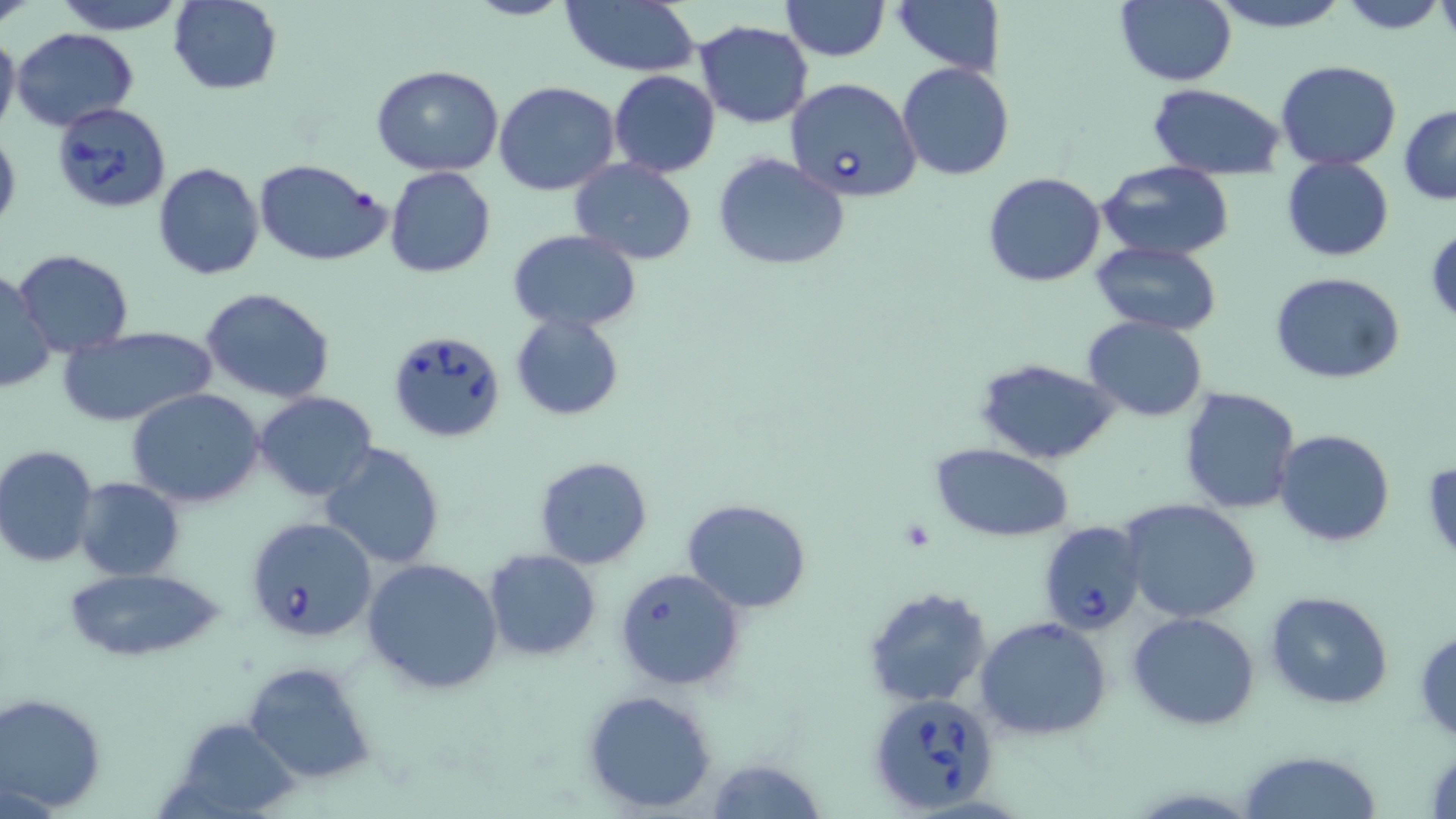
Approximate bounding boxes as (x1,y1)-(x2,y2) corner pairs in pixels. Uninfected red blood cell locations: (0,0)-(36,27), (50,0)-(191,35), (168,0)-(283,94), (465,0)-(571,22), (780,0)-(888,61), (893,0)-(1005,75), (1115,0)-(1237,86), (1204,0)-(1352,33), (1338,0)-(1449,34), (559,2)-(702,77), (693,20)-(814,128), (0,27)-(21,141), (10,27)-(140,132), (1276,59)-(1402,169), (897,62)-(1015,182), (371,65)-(505,177), (609,70)-(720,178), (494,81)-(621,196), (1148,84)-(1285,180), (1398,105)-(1456,204), (714,153)-(849,271), (1282,157)-(1393,262), (254,159)-(392,267), (153,160)-(264,281), (571,160)-(698,264), (1096,160)-(1235,262), (385,167)-(496,279), (984,173)-(1106,288), (1425,225)-(1456,330), (507,229)-(642,334), (1091,240)-(1223,337), (12,249)-(135,356), (0,268)-(56,397), (1270,270)-(1406,385), (200,288)-(335,404), (510,311)-(626,421), (1083,315)-(1207,420), (58,325)-(217,429), (974,358)-(1118,464), (125,387)-(265,509), (1177,387)-(1301,515), (256,391)-(378,502), (1272,429)-(1397,547), (319,441)-(445,570), (932,443)-(1074,542), (1,444)-(100,567), (534,456)-(653,569), (73,477)-(186,581), (681,498)-(811,612), (1118,498)-(1261,622), (483,550)-(601,660), (361,557)-(504,693), (59,564)-(230,663), (614,567)-(745,690), (863,585)-(994,709), (1265,591)-(1393,710), (1127,611)-(1261,730), (976,616)-(1112,740), (1413,626)-(1456,743), (241,658)-(376,788), (581,689)-(716,813), (0,691)-(106,814), (172,717)-(302,818), (1237,750)-(1381,819), (706,757)-(828,819). Babesia divergens-infected red blood cell locations: (784,76)-(922,203), (51,101)-(172,215), (385,329)-(507,442), (246,516)-(378,645), (1034,519)-(1146,636), (867,692)-(1000,814). Slide-level diagnosis: Babesia divergens. Image is 1456×819 pixels. Thin blood film. 1000x magnification. May-Grünwald-Giemsa stain. Light microscopy. One field of a larger specimen.